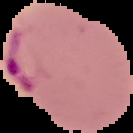

Summary:
  - Preparation: thin blood film
  - Image type: segmented cell region on a black background
  - Image size: 133×133 pixels
  - Malaria status: parasitized